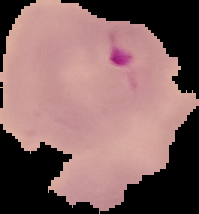

Summary:
  - Preparation: thin blood smear
  - Image type: cell region segmented out of the field of view; surrounding area masked to black
  - Image size: 199×214 pixels
  - Malaria status: parasitized